Name the blood parasite species.
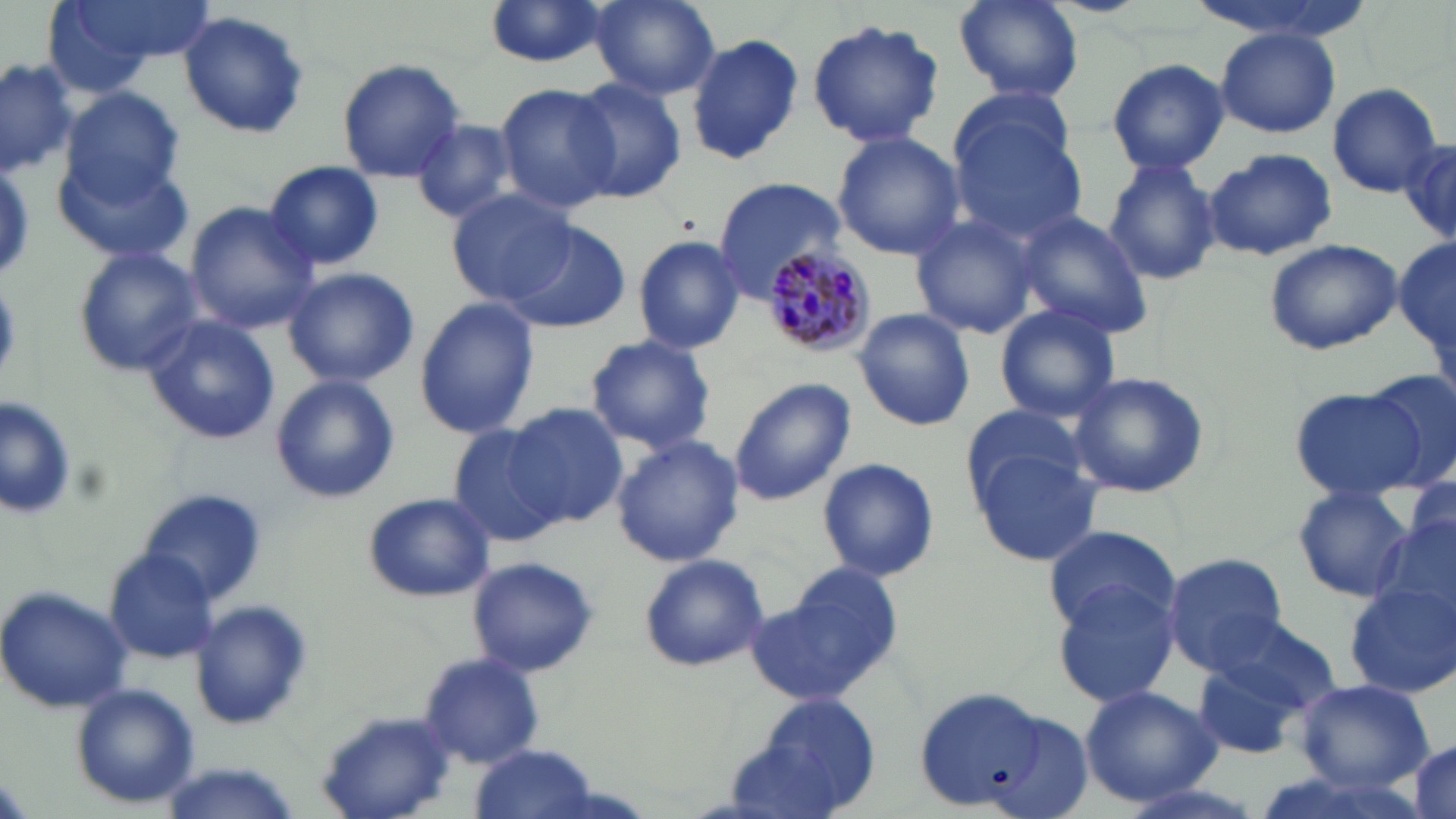

Plasmodium malariae.

{
  "stain": "May-Grünwald-Giemsa",
  "preparation": "thin blood smear",
  "modality": "optical microscopy",
  "image_size": "1456×819 pixels",
  "uninfected_red_blood_cell_locations": "approximate bounding boxes as named x1/y1/x2/y2 corners in pixels: (x1=39, y1=0, x2=202, y2=88), (x1=952, y1=0, x2=1085, y2=105), (x1=588, y1=1, x2=719, y2=99), (x1=483, y1=3, x2=613, y2=71), (x1=177, y1=10, x2=312, y2=141), (x1=806, y1=17, x2=946, y2=149), (x1=1215, y1=27, x2=1343, y2=139), (x1=686, y1=32, x2=803, y2=168), (x1=0, y1=57, x2=79, y2=175), (x1=336, y1=58, x2=468, y2=183), (x1=1106, y1=59, x2=1230, y2=174), (x1=568, y1=78, x2=689, y2=203), (x1=495, y1=83, x2=623, y2=212), (x1=1326, y1=83, x2=1443, y2=195), (x1=60, y1=87, x2=185, y2=208), (x1=948, y1=110, x2=1090, y2=245), (x1=409, y1=117, x2=525, y2=224), (x1=832, y1=132, x2=964, y2=260), (x1=1399, y1=142, x2=1455, y2=248), (x1=1203, y1=148, x2=1339, y2=262), (x1=57, y1=151, x2=189, y2=264), (x1=1102, y1=156, x2=1220, y2=285), (x1=262, y1=159, x2=384, y2=272), (x1=714, y1=178, x2=846, y2=292), (x1=448, y1=189, x2=578, y2=307), (x1=183, y1=202, x2=320, y2=334), (x1=1014, y1=210, x2=1153, y2=337), (x1=909, y1=215, x2=1038, y2=339), (x1=503, y1=218, x2=629, y2=334), (x1=630, y1=234, x2=746, y2=353), (x1=1262, y1=238, x2=1403, y2=356), (x1=1396, y1=238, x2=1454, y2=349), (x1=72, y1=247, x2=202, y2=374), (x1=283, y1=267, x2=418, y2=387), (x1=413, y1=299, x2=540, y2=439), (x1=994, y1=303, x2=1122, y2=423), (x1=852, y1=308, x2=976, y2=431), (x1=141, y1=313, x2=283, y2=445), (x1=584, y1=334, x2=718, y2=454), (x1=1067, y1=369, x2=1211, y2=499), (x1=1363, y1=369, x2=1456, y2=488), (x1=269, y1=374, x2=400, y2=504), (x1=727, y1=378, x2=856, y2=506), (x1=1289, y1=388, x2=1427, y2=499), (x1=1, y1=396, x2=78, y2=521), (x1=956, y1=402, x2=1095, y2=507), (x1=504, y1=403, x2=626, y2=527), (x1=446, y1=424, x2=567, y2=549), (x1=610, y1=434, x2=743, y2=568), (x1=969, y1=448, x2=1102, y2=566), (x1=815, y1=456, x2=940, y2=582), (x1=1292, y1=483, x2=1414, y2=604), (x1=137, y1=487, x2=265, y2=603), (x1=363, y1=490, x2=493, y2=602), (x1=1377, y1=508, x2=1456, y2=630), (x1=1042, y1=523, x2=1179, y2=635), (x1=104, y1=547, x2=219, y2=662), (x1=1162, y1=551, x2=1288, y2=674), (x1=639, y1=555, x2=769, y2=672), (x1=467, y1=557, x2=600, y2=679), (x1=746, y1=572, x2=904, y2=712), (x1=1049, y1=576, x2=1181, y2=710), (x1=1344, y1=579, x2=1456, y2=700), (x1=0, y1=586, x2=133, y2=715), (x1=192, y1=601, x2=311, y2=729), (x1=1202, y1=618, x2=1341, y2=726), (x1=1190, y1=652, x2=1314, y2=761), (x1=417, y1=654, x2=545, y2=767), (x1=1297, y1=680, x2=1434, y2=788), (x1=1078, y1=683, x2=1222, y2=807), (x1=71, y1=685, x2=200, y2=809), (x1=913, y1=686, x2=1054, y2=811), (x1=736, y1=690, x2=886, y2=819), (x1=317, y1=708, x2=456, y2=816), (x1=1408, y1=741, x2=1453, y2=817), (x1=471, y1=746, x2=599, y2=819)",
  "magnification": "1000x",
  "field_of_view": "one of a larger specimen",
  "plasmodium_malariae_infected_red_blood_cell_locations": "approximate bounding boxes as named x1/y1/x2/y2 corners in pixels: (x1=762, y1=241, x2=877, y2=359)"
}